Point out each leukocyte.
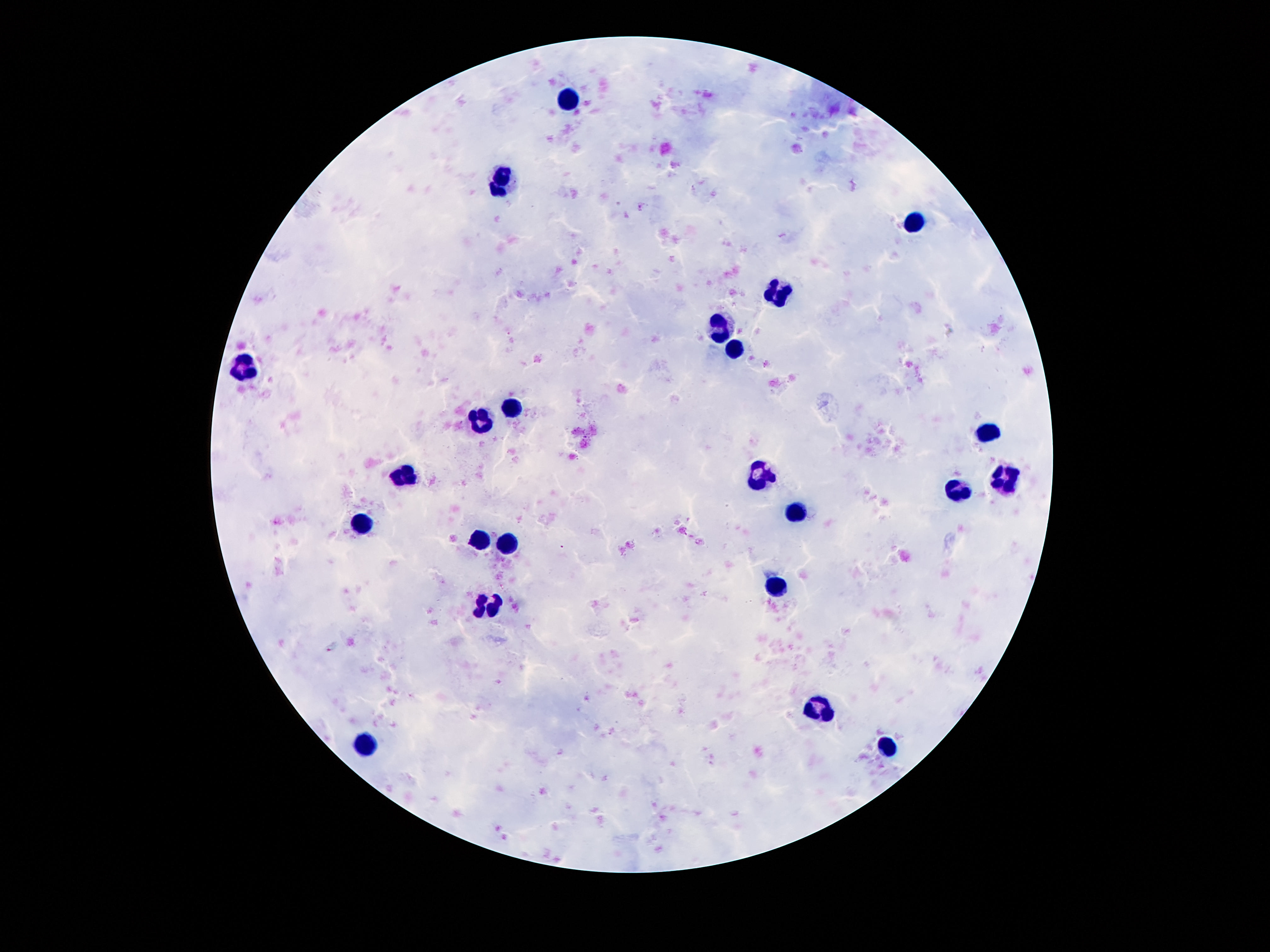

Approximate centers as {x, y} in pixels.
Leukocytes: {570, 97}, {502, 183}, {919, 218}, {782, 293}, {721, 329}, {737, 350}, {241, 367}, {513, 407}, {481, 421}, {987, 431}, {1004, 475}, {402, 479}, {759, 479}, {959, 493}, {796, 514}, {360, 524}, {479, 539}, {506, 545}, {775, 587}, {488, 606}, {815, 709}, {366, 743}, {887, 748}.

Summary:
  - Stain: Giemsa
  - Patient malaria status: negative
  - Preparation: thick blood smear
  - Image size: 1270×952 pixels
  - Magnification: 100x
  - Capture: smartphone camera through the microscope eyepiece
  - Field of view: single